Locate every blood parasite and identify its species.
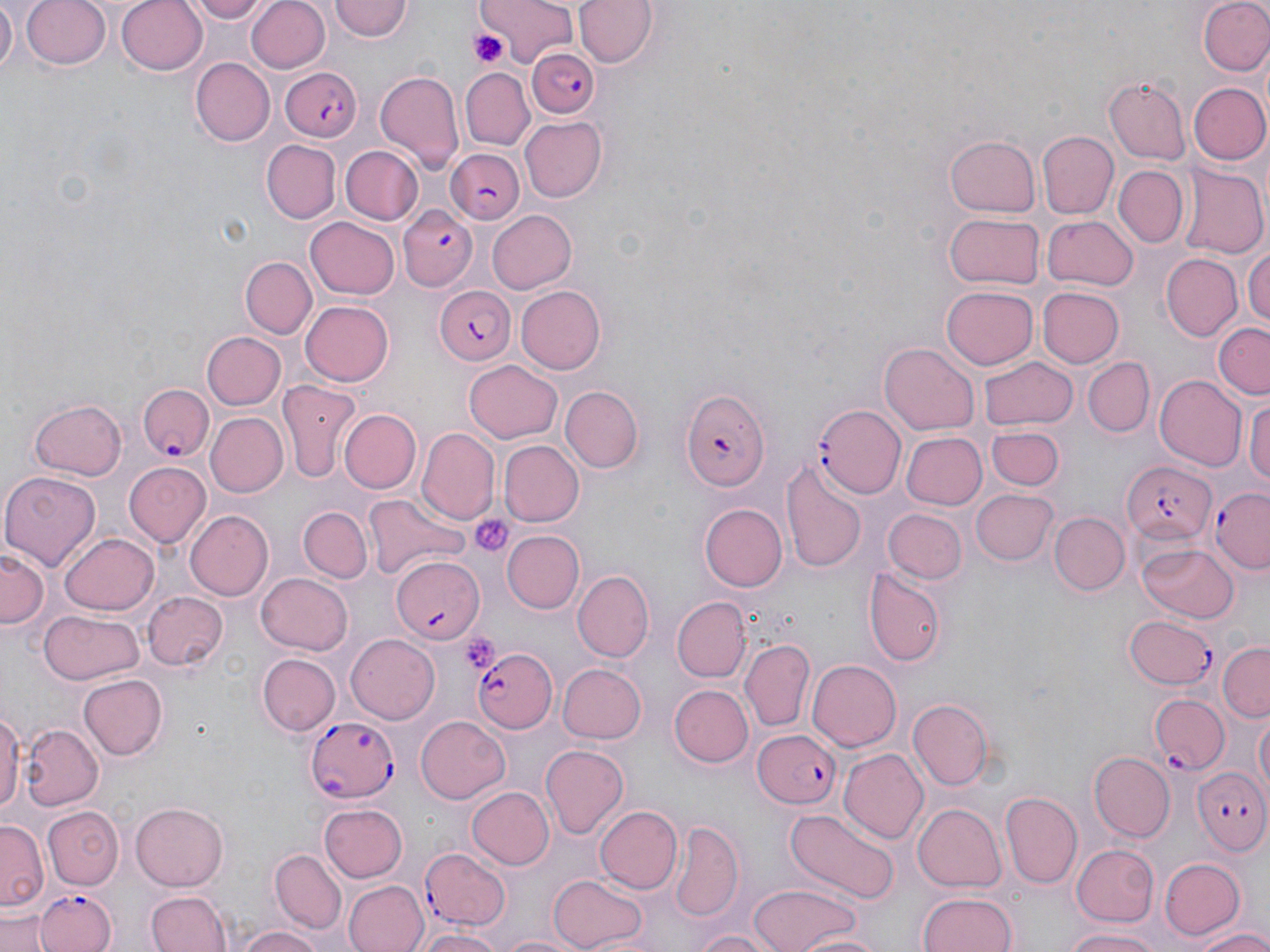
Approximate bounding boxes as (x1, y1, x2, y2) in pixels.
Plasmodium falciparum-infected red blood cells: (527, 47, 599, 120), (282, 67, 364, 142), (444, 148, 526, 224), (396, 205, 478, 292), (432, 285, 515, 364), (137, 383, 213, 462), (679, 389, 770, 495), (815, 404, 905, 499), (1120, 462, 1216, 544), (1210, 487, 1269, 574), (391, 556, 483, 641), (1123, 615, 1218, 691), (472, 645, 558, 734), (1150, 692, 1229, 774), (306, 714, 399, 803), (753, 729, 842, 810), (1191, 762, 1270, 854), (421, 848, 512, 930), (34, 887, 115, 951).
No Plasmodium ovale, Plasmodium malariae, Plasmodium vivax, Babesia divergens, or Trypanosoma brucei observed.

Summary:
  - Uninfected red blood cell locations: (1, 0, 17, 76), (22, 0, 112, 71), (116, 0, 209, 76), (187, 0, 272, 24), (479, 0, 581, 65), (575, 0, 657, 68), (1199, 0, 1270, 77), (248, 1, 330, 73), (329, 1, 413, 44), (191, 58, 275, 144), (460, 67, 536, 149), (375, 71, 464, 172), (1104, 77, 1192, 164), (1186, 82, 1270, 166), (519, 115, 606, 200), (1038, 132, 1118, 218), (947, 134, 1040, 218), (263, 140, 340, 223), (341, 145, 423, 224), (1112, 164, 1188, 247), (1177, 165, 1270, 260), (487, 208, 575, 292), (944, 211, 1044, 290), (1042, 214, 1138, 290), (305, 217, 398, 300), (1244, 239, 1270, 334), (1160, 253, 1242, 342), (240, 256, 317, 338), (517, 286, 606, 374), (941, 286, 1038, 369), (1038, 286, 1126, 368), (301, 299, 395, 387), (1212, 324, 1270, 397), (202, 332, 286, 410), (880, 342, 978, 435), (978, 355, 1076, 431), (1082, 356, 1155, 435), (466, 359, 563, 441), (1154, 374, 1247, 471), (275, 382, 360, 484), (561, 385, 643, 472), (1247, 390, 1270, 496), (28, 397, 127, 480), (338, 408, 419, 493), (205, 412, 288, 498), (986, 426, 1064, 490), (419, 429, 498, 522), (900, 431, 986, 511), (499, 440, 583, 525), (780, 458, 866, 573), (123, 463, 210, 548), (0, 470, 100, 570), (970, 488, 1057, 566), (366, 492, 469, 583), (699, 502, 787, 591), (299, 507, 370, 582), (185, 509, 272, 598), (885, 510, 964, 583), (1049, 510, 1128, 594), (502, 530, 584, 614), (60, 534, 159, 615), (1136, 543, 1239, 623), (0, 548, 49, 627), (863, 566, 947, 667), (573, 570, 652, 662), (255, 572, 351, 656), (141, 591, 227, 671), (673, 599, 748, 681), (39, 611, 143, 686), (345, 634, 438, 724), (741, 638, 814, 732), (1217, 643, 1270, 719), (258, 654, 340, 736), (806, 658, 901, 751), (555, 662, 646, 745), (78, 674, 167, 761), (669, 685, 754, 768), (909, 699, 994, 788), (0, 707, 22, 818), (1249, 711, 1270, 802), (414, 714, 511, 802), (20, 724, 101, 811), (540, 745, 631, 840), (838, 749, 925, 841), (1089, 751, 1176, 841), (468, 786, 553, 868), (1001, 791, 1082, 887), (132, 800, 228, 889), (914, 803, 1006, 890), (319, 804, 409, 882), (595, 805, 681, 895), (43, 807, 123, 890), (787, 808, 897, 903), (671, 821, 743, 920), (1, 822, 45, 913), (1071, 844, 1158, 927), (271, 850, 346, 932), (1159, 857, 1244, 940), (550, 873, 649, 950), (343, 879, 427, 952), (750, 883, 860, 952), (145, 887, 233, 952), (917, 889, 1019, 951), (0, 911, 51, 952), (234, 926, 326, 952), (1063, 926, 1162, 952), (415, 928, 503, 952), (688, 928, 785, 952), (1190, 929, 1270, 952), (495, 931, 591, 952), (797, 931, 885, 952)
  - Platelet locations: (468, 27, 511, 67), (472, 513, 514, 558), (459, 633, 502, 673)
  - Slide-level diagnosis: Plasmodium falciparum
  - Image size: 1270×952 pixels
  - Field of view: one of a larger specimen
  - Stain: May-Grünwald-Giemsa
  - Magnification: 1000x
  - Modality: light microscopy
  - Preparation: thin blood smear